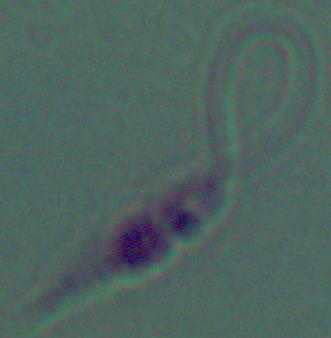
Summary:
  - Modality: photomicrograph
  - Magnification: 1000x
  - Identification: Leishmania